Report the malaria status of this cell.
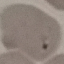
Parasitized.

Summary:
  - Capture: smartphone camera at the microscope eyepiece
  - Stain: Giemsa
  - Preparation: thin blood smear
  - Image type: cell patch, automatically extracted from a larger field of view and resized to 64 × 64 pixels